Assess the morphology of the erythrocytes.
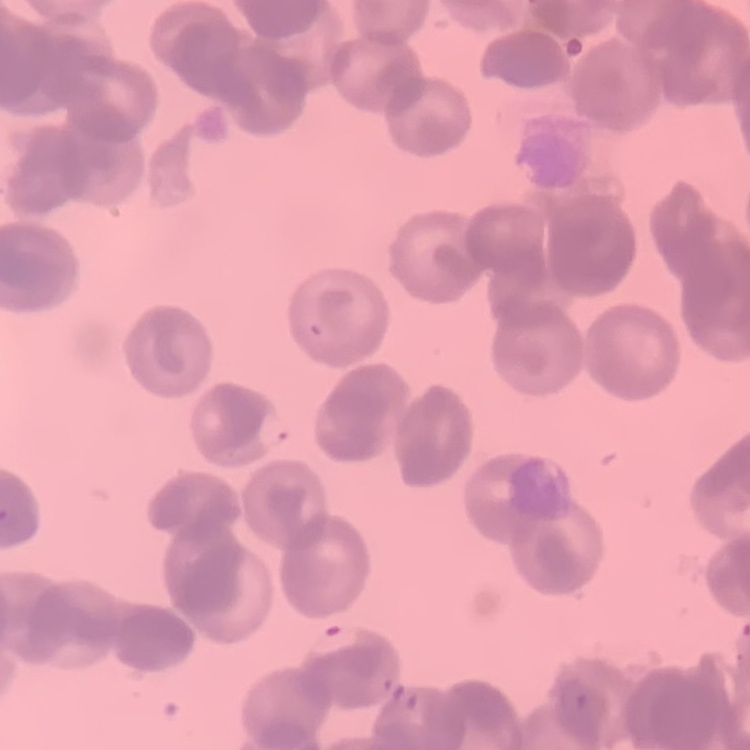
They show rouleaux formation.

stain = Field's or Giemsa
preparation = thin blood film
image type = one tile cut from a larger photomicrograph